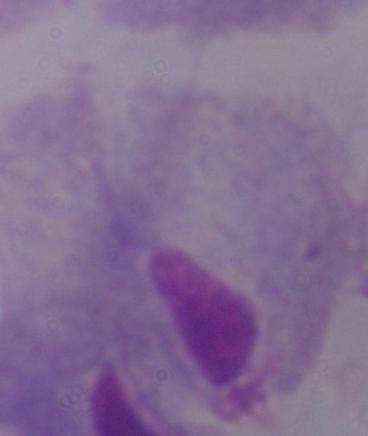

1000x magnification. A trichomonad is shown. Micrograph.